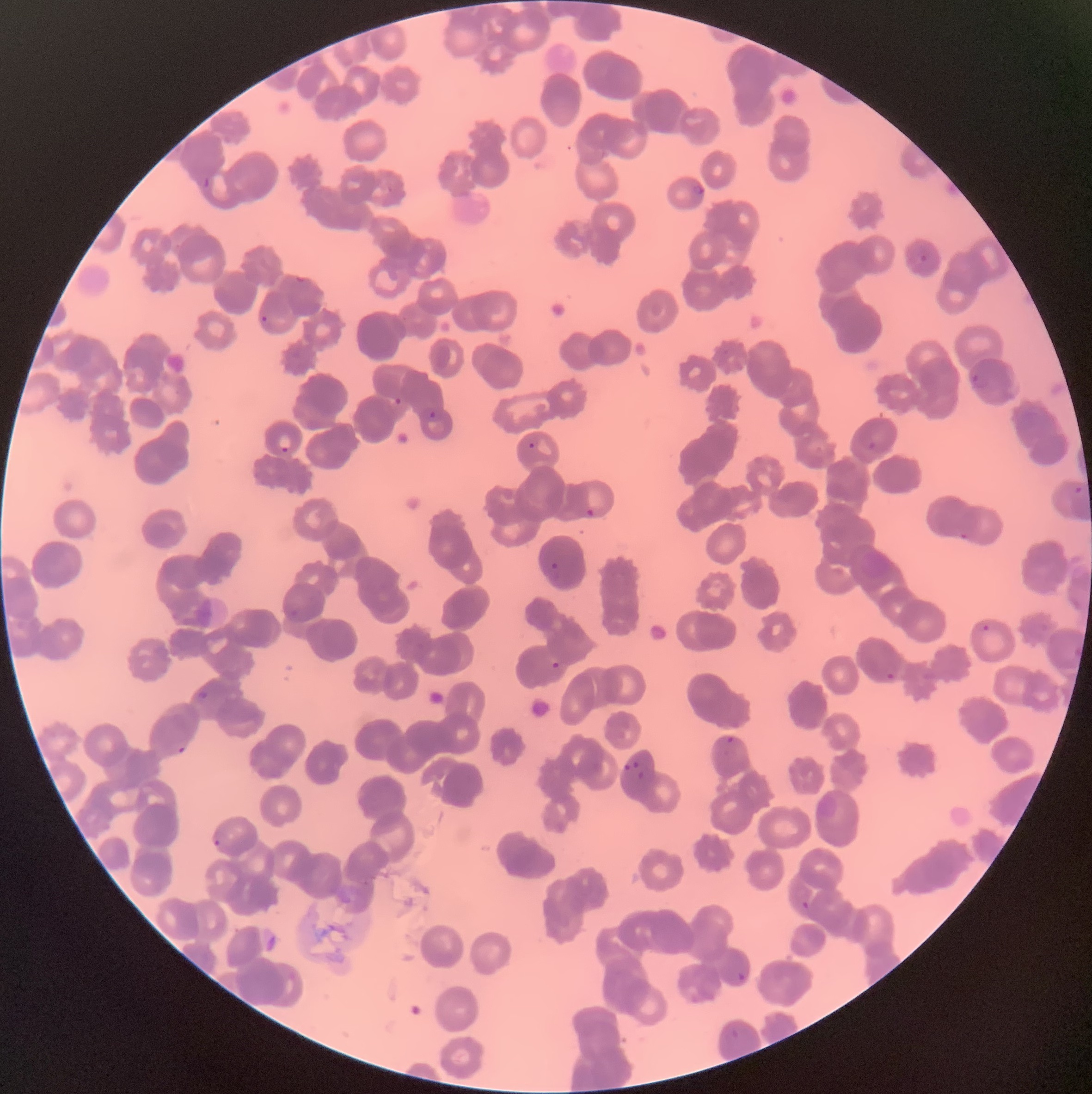
{
  "preparation": "thin blood smear",
  "plasmodium_parasite_locations": "approximate bounding boxes as named x1/y1/x2/y2 corners in pixels: (x1=203, y1=175, x2=211, y2=190), (x1=692, y1=184, x2=704, y2=196), (x1=919, y1=254, x2=929, y2=262), (x1=261, y1=315, x2=269, y2=323), (x1=971, y1=372, x2=990, y2=389), (x1=394, y1=397, x2=403, y2=406), (x1=429, y1=411, x2=436, y2=419), (x1=867, y1=441, x2=885, y2=455), (x1=527, y1=442, x2=535, y2=449), (x1=280, y1=446, x2=289, y2=453), (x1=1073, y1=485, x2=1083, y2=495), (x1=585, y1=508, x2=595, y2=519), (x1=958, y1=531, x2=970, y2=540), (x1=547, y1=562, x2=560, y2=582), (x1=981, y1=624, x2=990, y2=632), (x1=1074, y1=646, x2=1082, y2=659), (x1=551, y1=661, x2=560, y2=669), (x1=886, y1=672, x2=895, y2=681), (x1=196, y1=689, x2=208, y2=703), (x1=725, y1=736, x2=735, y2=747), (x1=177, y1=745, x2=187, y2=754), (x1=622, y1=761, x2=641, y2=770), (x1=637, y1=771, x2=645, y2=778), (x1=213, y1=839, x2=221, y2=848), (x1=801, y1=901, x2=810, y2=910), (x1=737, y1=971, x2=747, y2=982), (x1=730, y1=1029, x2=741, y2=1040)",
  "modality": "optical microscopy",
  "red_blood_cell_morphology": "rouleaux formation",
  "image_size": "1092×1094 pixels"
}